Identify the parasite.
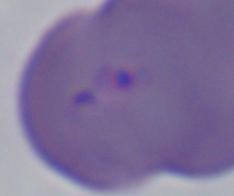

This is Babesia.

Photomicrograph. Captured at 1000x magnification.